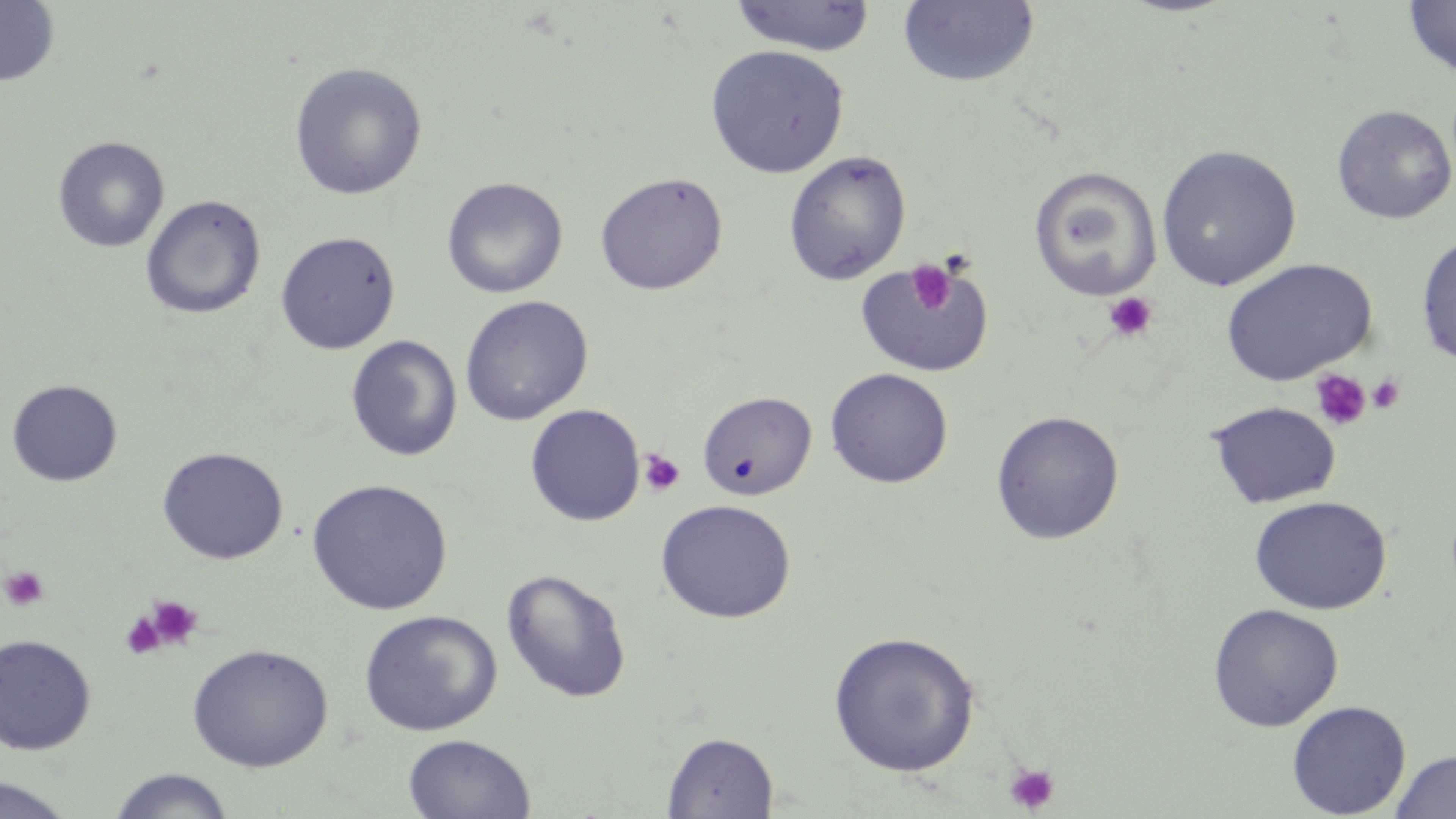

Summary:
  - Coordinate format: approximate bounding boxes as [x1, y1, x2, y2] in pixels
  - Uninfected red blood cell locations: [0, 0, 60, 87], [1403, 0, 1456, 78], [729, 1, 877, 56], [897, 1, 1040, 88], [705, 44, 849, 178], [289, 61, 427, 200], [1332, 104, 1456, 224], [52, 135, 170, 253], [1156, 144, 1302, 292], [783, 151, 911, 286], [1028, 165, 1163, 301], [594, 171, 728, 295], [442, 177, 568, 299], [140, 194, 267, 320], [1415, 230, 1456, 367], [275, 231, 400, 354], [854, 256, 993, 378], [1219, 258, 1377, 386], [459, 295, 594, 425], [346, 335, 463, 461], [825, 367, 953, 488], [6, 379, 124, 487], [697, 391, 817, 500], [1207, 400, 1341, 509], [525, 404, 645, 527], [990, 410, 1125, 545], [156, 446, 288, 564], [307, 478, 453, 615], [1249, 495, 1392, 615], [655, 499, 796, 623], [501, 568, 633, 703], [1207, 603, 1344, 731], [359, 609, 503, 736], [827, 630, 981, 777], [0, 633, 97, 754], [187, 642, 333, 772], [1286, 699, 1412, 818], [661, 731, 778, 817], [402, 733, 536, 818], [1389, 749, 1456, 819], [106, 768, 237, 818], [0, 774, 79, 819]
  - Platelet locations: [906, 261, 957, 315], [1103, 292, 1160, 343], [1309, 369, 1372, 432], [1368, 374, 1406, 414], [638, 449, 685, 497], [1, 565, 51, 611], [146, 596, 202, 650], [120, 611, 164, 660], [1004, 762, 1060, 814]
  - Slide-level diagnosis: negative for blood parasites
  - Magnification: 1000x
  - Modality: light microscopy
  - Field of view: one of a larger specimen
  - Image size: 1456×819 pixels
  - Stain: May-Grünwald-Giemsa
  - Preparation: thin blood smear